Assess this cell for malaria.
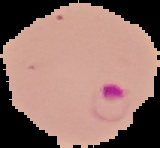
It is parasitized.

Cell region segmented out of the field of view; the surrounding area is masked to black. From a thin blood smear. Image is 160×148 pixels.